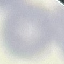
Summary:
  - Result: no malaria parasites seen
  - Stain: Giemsa
  - Image type: cell patch, automatically extracted from a larger field of view and resized to 64 × 64 pixels
  - Capture: smartphone through the microscope eyepiece
  - Preparation: thin blood film